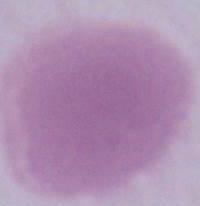 Photomicrograph. Captured at 1000x magnification. A red blood cell is seen.